Give the position of every malaria parasite.
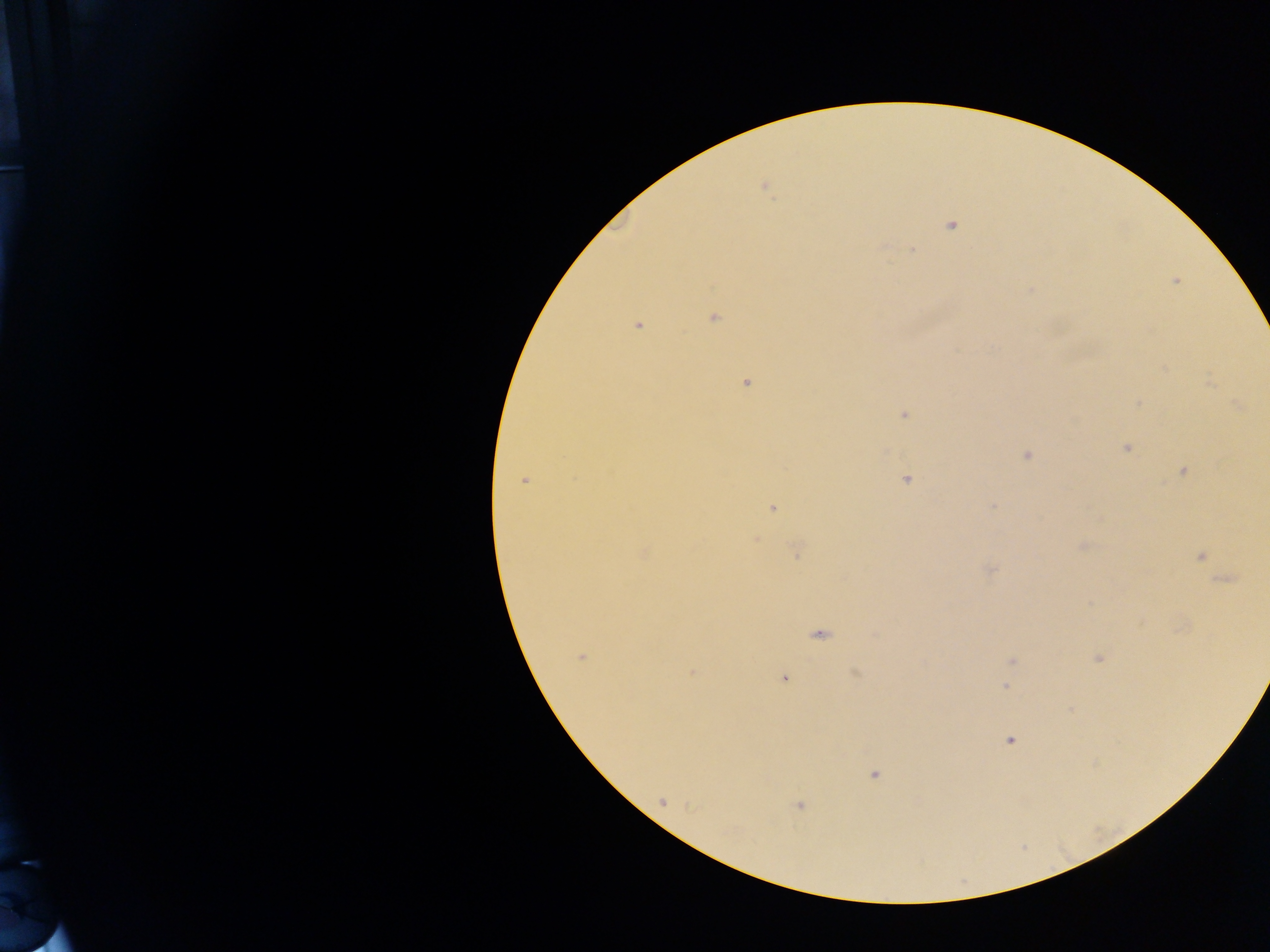
Approximate centers as x y in pixels.
Malaria parasites: 951 226; 912 248; 713 318; 639 325; 746 384; 1137 402; 903 416; 1124 449; 1181 470; 525 480; 906 480; 993 504; 773 508; 796 552; 817 633; 582 657; 1098 658; 854 673; 784 679; 1005 685; 1010 740; 876 774; 800 805.

One field of view. Collected in Ghana. Thick blood film. Photographed through a microscope with a mobile-phone camera. Image is 1270×952 pixels.